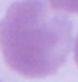

Photomicrograph. 1000x magnification. An erythrocyte is shown.